Point out each Plasmodium parasite.
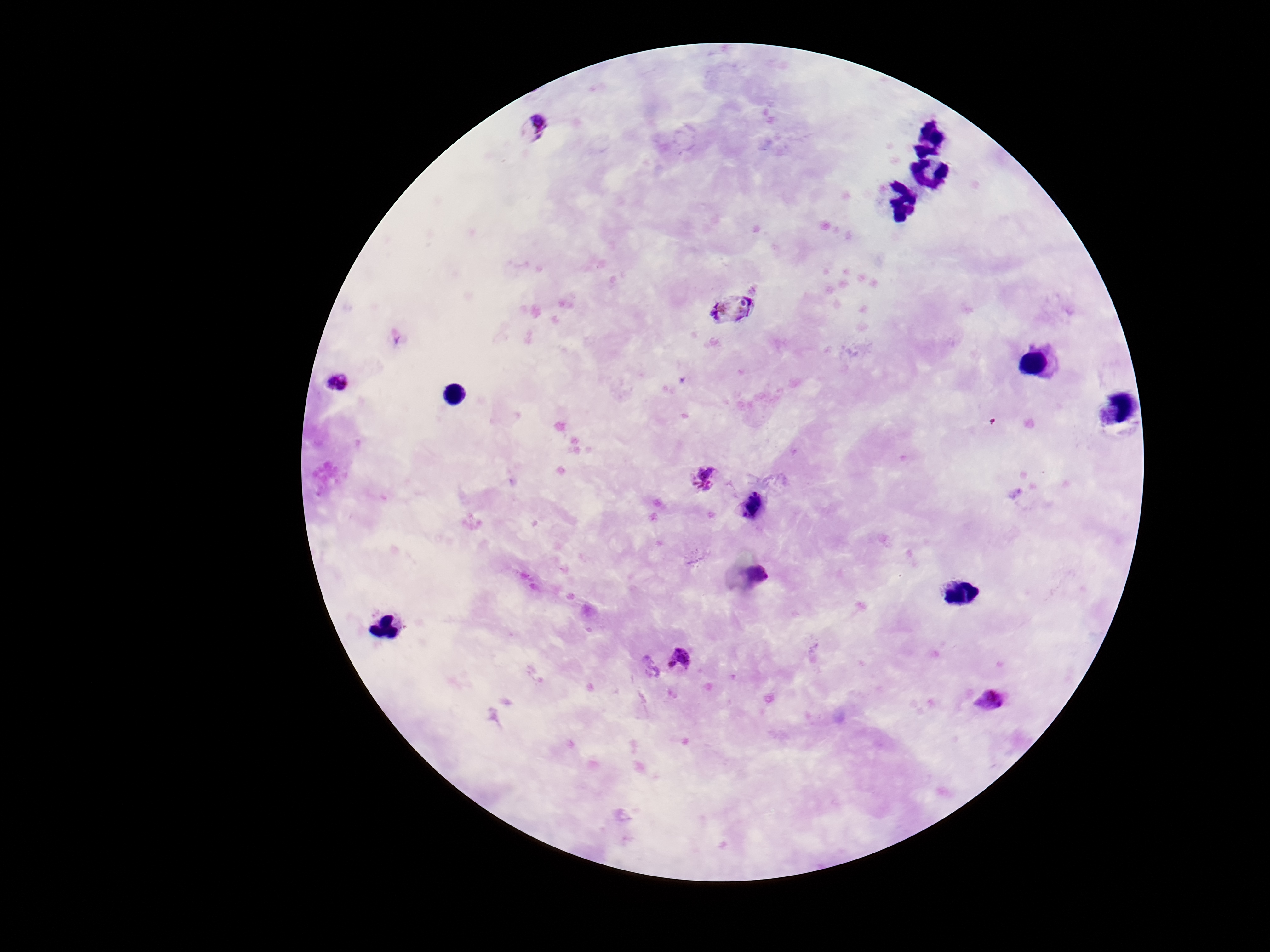

Approximate centers as {x, y} in pixels.
Plasmodium parasites: {535, 126}, {732, 311}, {340, 387}, {705, 479}, {753, 505}, {759, 575}, {680, 659}, {988, 701}.

Image is 1270×952 pixels. Patient malaria status: positive. Giemsa-stained preparation. Thick blood film. Photographed through the microscope eyepiece with a smartphone camera. 100x magnification. Single field of view.